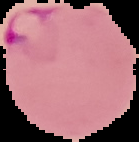

{
  "result": "malaria parasites detected",
  "preparation": "thin blood film",
  "image_type": "cell region segmented out of the field of view; surrounding area masked to black",
  "image_size": "139×142 pixels"
}